Name the blood parasite species.
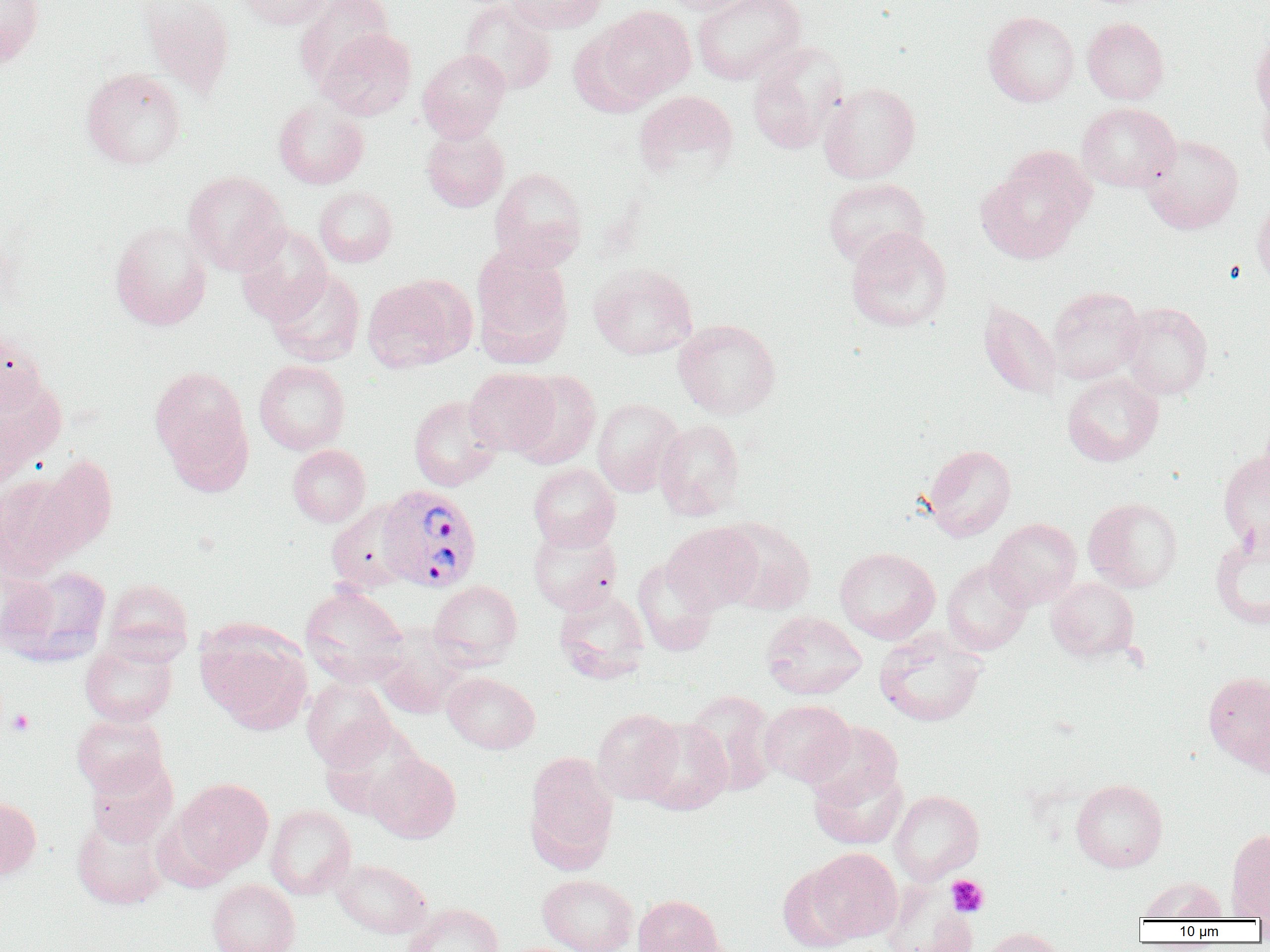

Plasmodium vivax.

Approximate bounding boxes as (x1,y1)-(x2,y2) corner pairs in pixels. Platelet locations: (7,708)-(35,736), (946,875)-(989,917). Uninfected red blood cell locations: (0,0)-(45,68), (137,0)-(236,98), (235,0)-(333,29), (293,0)-(394,89), (504,0)-(608,33), (659,0)-(761,15), (692,0)-(806,84), (459,1)-(557,95), (596,6)-(696,104), (983,11)-(1080,107), (1083,17)-(1169,104), (316,28)-(417,121), (568,28)-(656,116), (1250,30)-(1270,123), (746,42)-(848,155), (418,48)-(510,142), (81,68)-(186,170), (819,81)-(921,183), (1258,88)-(1270,172), (633,89)-(738,182), (273,98)-(369,189), (1076,103)-(1181,192), (421,126)-(509,212), (1141,135)-(1243,234), (976,149)-(1093,265), (489,167)-(587,270), (183,171)-(289,275), (822,177)-(930,269), (314,186)-(397,267), (1252,195)-(1270,291), (110,220)-(212,330), (236,224)-(332,324), (846,226)-(951,332), (471,246)-(573,363), (588,262)-(697,360), (266,268)-(365,366), (362,277)-(469,372), (1047,286)-(1145,384), (978,299)-(1062,400), (1119,302)-(1213,399), (673,319)-(781,420), (0,331)-(49,419), (254,359)-(350,454), (149,365)-(251,479), (464,367)-(560,457), (509,371)-(601,469), (0,373)-(66,475), (1062,373)-(1163,466), (409,396)-(501,491), (592,398)-(683,497), (654,420)-(745,520), (287,444)-(370,527), (924,444)-(1016,541), (1218,451)-(1270,550), (33,455)-(117,558), (528,463)-(621,551), (0,474)-(83,579), (1084,497)-(1183,593), (326,501)-(414,593), (717,517)-(816,615), (987,518)-(1082,609), (663,523)-(761,614), (527,524)-(622,615), (1210,528)-(1270,630), (835,547)-(940,644), (632,558)-(718,655), (942,559)-(1033,655), (2,564)-(112,666), (1047,577)-(1140,662), (102,578)-(193,662), (428,580)-(522,668), (300,585)-(409,685), (554,590)-(650,683), (760,610)-(868,699), (195,621)-(312,733), (874,629)-(988,727), (372,631)-(468,719), (80,638)-(178,727), (1203,671)-(1270,773), (442,672)-(540,754), (301,676)-(396,770), (683,690)-(781,796), (759,699)-(855,787), (592,708)-(683,804), (71,712)-(169,797), (637,718)-(731,815), (320,721)-(425,819), (806,721)-(903,809), (524,751)-(618,871), (366,752)-(461,843), (85,756)-(177,847), (809,765)-(907,850), (173,778)-(274,875), (1071,778)-(1168,872), (889,790)-(984,884), (0,795)-(42,879), (266,804)-(356,899), (71,812)-(171,910), (1226,828)-(1270,919), (805,847)-(902,943), (331,859)-(432,938), (777,864)-(861,952), (538,874)-(638,952), (1137,876)-(1227,921), (207,879)-(300,952), (883,881)-(978,952), (632,894)-(726,952), (404,903)-(504,952), (975,927)-(1066,952). Plasmodium vivax-infected red blood cell locations: (377,484)-(483,593). Optical microscopy. Thin blood film. 1000x magnification. Image is 1270×952 pixels. Single field of view.